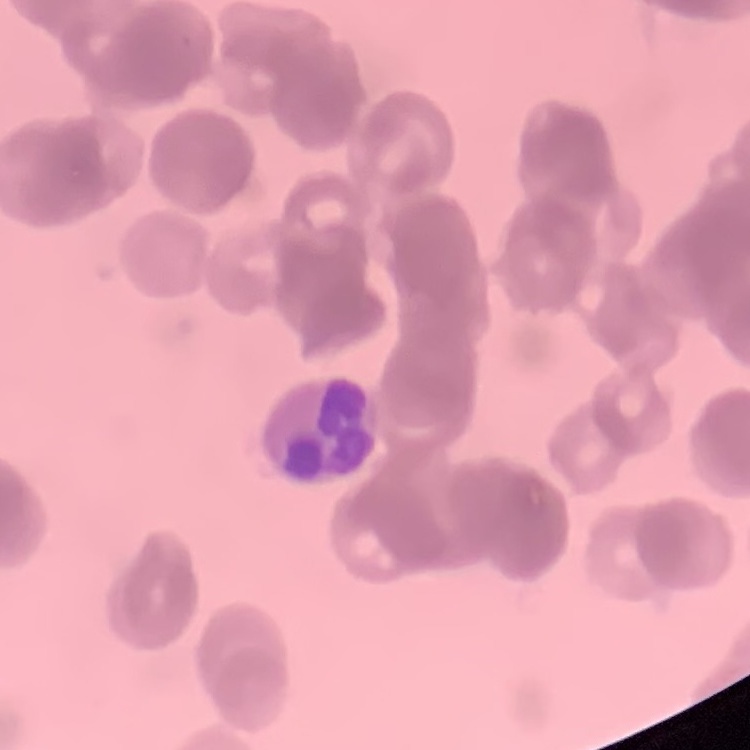

The erythrocytes exhibit rouleaux formation. Stained with either Field's or Giemsa. Thin blood film. One tile cut from a larger photomicrograph.